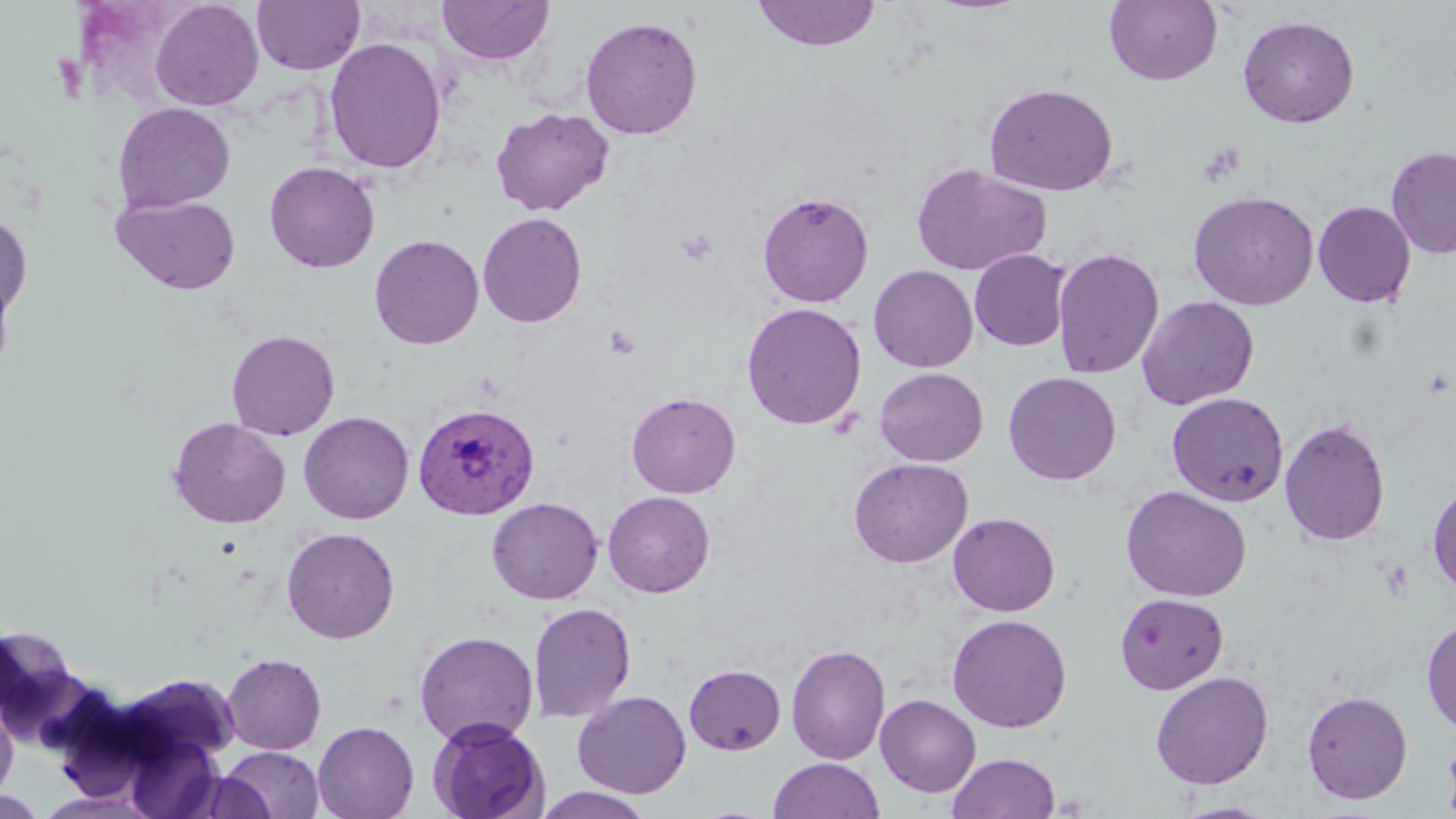
Approximate bounding boxes as (x1, y1, x2, y2) in pixels. Uninfected red blood cell locations: (752, 0, 881, 51), (1104, 0, 1222, 85), (150, 1, 264, 110), (251, 1, 365, 75), (436, 1, 555, 67), (580, 15, 704, 140), (1237, 15, 1360, 128), (323, 37, 447, 174), (983, 82, 1119, 196), (113, 102, 235, 213), (490, 106, 614, 217), (1386, 144, 1456, 259), (264, 161, 380, 273), (911, 163, 1052, 276), (1187, 189, 1319, 310), (757, 191, 874, 308), (111, 193, 242, 295), (1313, 200, 1416, 308), (0, 211, 33, 319), (477, 211, 587, 328), (369, 233, 484, 350), (1052, 246, 1164, 380), (969, 248, 1071, 351), (869, 264, 978, 373), (0, 267, 16, 382), (1137, 295, 1260, 410), (741, 302, 867, 430), (226, 329, 340, 440), (874, 367, 989, 467), (1003, 371, 1122, 485), (626, 391, 740, 498), (1166, 391, 1289, 508), (298, 411, 414, 524), (168, 417, 291, 529), (1279, 417, 1391, 547), (848, 457, 973, 568), (1427, 480, 1456, 597), (1119, 485, 1252, 602), (602, 491, 715, 598), (486, 497, 604, 605), (947, 512, 1060, 616), (281, 527, 400, 644), (1114, 592, 1229, 695), (528, 602, 637, 722), (947, 613, 1072, 733), (1421, 616, 1455, 735), (0, 622, 82, 735), (414, 630, 539, 746), (787, 643, 891, 765), (222, 653, 326, 754), (684, 663, 786, 755), (1150, 671, 1274, 790), (118, 673, 243, 765), (573, 690, 692, 798), (1302, 690, 1413, 804), (875, 694, 981, 797), (0, 695, 18, 802), (427, 718, 549, 819), (312, 721, 419, 819), (1442, 733, 1456, 819), (126, 737, 224, 819), (220, 746, 324, 818), (947, 752, 1060, 819), (769, 757, 883, 818), (188, 772, 276, 818), (533, 787, 656, 818), (0, 791, 48, 817), (35, 791, 161, 818), (1172, 800, 1280, 818). Plasmodium vivax-infected red blood cell locations: (412, 402, 541, 519). Platelet locations: (675, 229, 717, 266), (604, 325, 641, 359). Slide-level diagnosis: Plasmodium vivax. Optical microscopy. Single field of view. May-Grünwald-Giemsa-stained preparation. Image is 1456×819 pixels. Thin blood smear. Captured at 1000x magnification.